Give the extent of all Plasmodium falciparum-infected red blood cells.
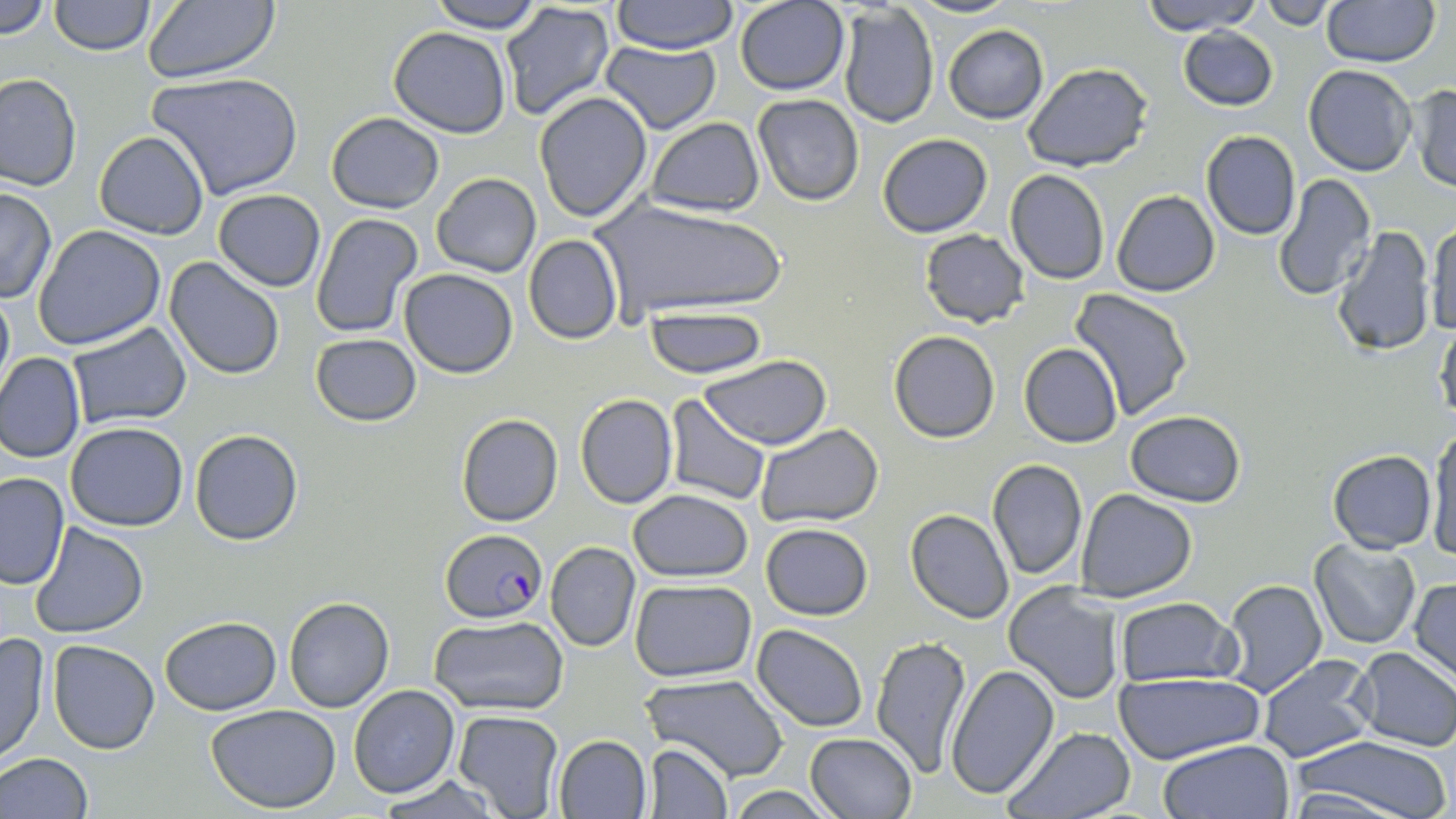

Approximate bounding boxes as named x1/y1/x2/y2 corners in pixels.
Plasmodium falciparum-infected red blood cells: (x1=441, y1=529, x2=547, y2=622).

Uninfected red blood cell locations: (x1=2, y1=0, x2=49, y2=37), (x1=49, y1=0, x2=155, y2=55), (x1=140, y1=0, x2=280, y2=83), (x1=425, y1=0, x2=543, y2=33), (x1=611, y1=0, x2=739, y2=54), (x1=906, y1=0, x2=1018, y2=19), (x1=1139, y1=0, x2=1261, y2=34), (x1=1259, y1=0, x2=1340, y2=29), (x1=1320, y1=0, x2=1439, y2=67), (x1=734, y1=1, x2=850, y2=96), (x1=498, y1=2, x2=616, y2=122), (x1=837, y1=5, x2=940, y2=128), (x1=943, y1=25, x2=1048, y2=124), (x1=387, y1=26, x2=510, y2=136), (x1=1177, y1=26, x2=1278, y2=111), (x1=599, y1=40, x2=721, y2=134), (x1=1022, y1=62, x2=1153, y2=170), (x1=1302, y1=64, x2=1416, y2=177), (x1=148, y1=72, x2=302, y2=201), (x1=1, y1=73, x2=80, y2=190), (x1=1407, y1=83, x2=1456, y2=192), (x1=533, y1=92, x2=652, y2=223), (x1=753, y1=93, x2=864, y2=205), (x1=327, y1=112, x2=444, y2=212), (x1=643, y1=117, x2=763, y2=217), (x1=95, y1=131, x2=209, y2=239), (x1=1201, y1=131, x2=1302, y2=239), (x1=876, y1=133, x2=993, y2=238), (x1=1005, y1=169, x2=1111, y2=284), (x1=1272, y1=173, x2=1377, y2=301), (x1=431, y1=174, x2=541, y2=276), (x1=0, y1=187, x2=56, y2=303), (x1=212, y1=190, x2=325, y2=292), (x1=1112, y1=190, x2=1220, y2=296), (x1=589, y1=196, x2=783, y2=323), (x1=309, y1=213, x2=423, y2=338), (x1=1426, y1=221, x2=1455, y2=338), (x1=1330, y1=224, x2=1437, y2=359), (x1=34, y1=225, x2=167, y2=349), (x1=919, y1=229, x2=1031, y2=328), (x1=522, y1=235, x2=622, y2=344), (x1=165, y1=258, x2=284, y2=379), (x1=399, y1=269, x2=520, y2=378), (x1=0, y1=285, x2=14, y2=400), (x1=1068, y1=289, x2=1195, y2=422), (x1=645, y1=306, x2=769, y2=378), (x1=65, y1=321, x2=192, y2=430), (x1=1434, y1=321, x2=1456, y2=425), (x1=888, y1=330, x2=999, y2=443), (x1=311, y1=333, x2=422, y2=426), (x1=1019, y1=343, x2=1121, y2=448), (x1=0, y1=352, x2=85, y2=463), (x1=700, y1=356, x2=833, y2=449), (x1=575, y1=393, x2=679, y2=509), (x1=665, y1=394, x2=770, y2=505), (x1=1124, y1=410, x2=1248, y2=506), (x1=456, y1=413, x2=563, y2=527), (x1=65, y1=422, x2=190, y2=531), (x1=755, y1=423, x2=884, y2=530), (x1=1426, y1=426, x2=1455, y2=559), (x1=190, y1=428, x2=303, y2=546), (x1=1328, y1=449, x2=1437, y2=553), (x1=987, y1=458, x2=1088, y2=579), (x1=1, y1=472, x2=70, y2=590), (x1=628, y1=488, x2=753, y2=583), (x1=1075, y1=488, x2=1197, y2=602), (x1=905, y1=509, x2=1013, y2=624), (x1=29, y1=523, x2=147, y2=638), (x1=761, y1=523, x2=873, y2=621), (x1=1309, y1=538, x2=1422, y2=649), (x1=546, y1=541, x2=641, y2=651), (x1=1221, y1=577, x2=1327, y2=698), (x1=629, y1=578, x2=757, y2=682), (x1=1408, y1=578, x2=1456, y2=683), (x1=1004, y1=580, x2=1125, y2=703), (x1=284, y1=596, x2=393, y2=713), (x1=1114, y1=596, x2=1239, y2=687), (x1=160, y1=615, x2=282, y2=715), (x1=428, y1=617, x2=570, y2=715), (x1=751, y1=624, x2=869, y2=731), (x1=0, y1=630, x2=50, y2=768), (x1=869, y1=635, x2=971, y2=777), (x1=48, y1=639, x2=159, y2=754), (x1=1350, y1=647, x2=1456, y2=751), (x1=1255, y1=652, x2=1380, y2=763), (x1=947, y1=663, x2=1060, y2=799), (x1=1115, y1=672, x2=1264, y2=762), (x1=642, y1=674, x2=791, y2=783), (x1=348, y1=685, x2=460, y2=798), (x1=206, y1=703, x2=342, y2=813), (x1=452, y1=710, x2=564, y2=819), (x1=1003, y1=727, x2=1138, y2=818), (x1=805, y1=733, x2=916, y2=819), (x1=553, y1=734, x2=651, y2=817), (x1=1290, y1=736, x2=1454, y2=819), (x1=1158, y1=738, x2=1296, y2=819), (x1=643, y1=743, x2=733, y2=817), (x1=0, y1=753, x2=93, y2=819), (x1=378, y1=779, x2=500, y2=817), (x1=723, y1=787, x2=840, y2=818). Slide-level diagnosis: Plasmodium falciparum. Thin blood film. May-Grünwald-Giemsa stain. Image is 1456×819 pixels. Light microscopy. 1000x magnification. Single field of view.